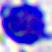
Captured at 400x magnification. Photomicrograph. A white blood cell is shown.